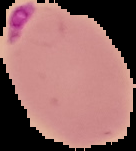
Summary:
  - Preparation: thin blood smear
  - Image size: 136×151 pixels
  - Image type: segmented cell region on a black background
  - Malaria status: parasitized